Locate platelets.
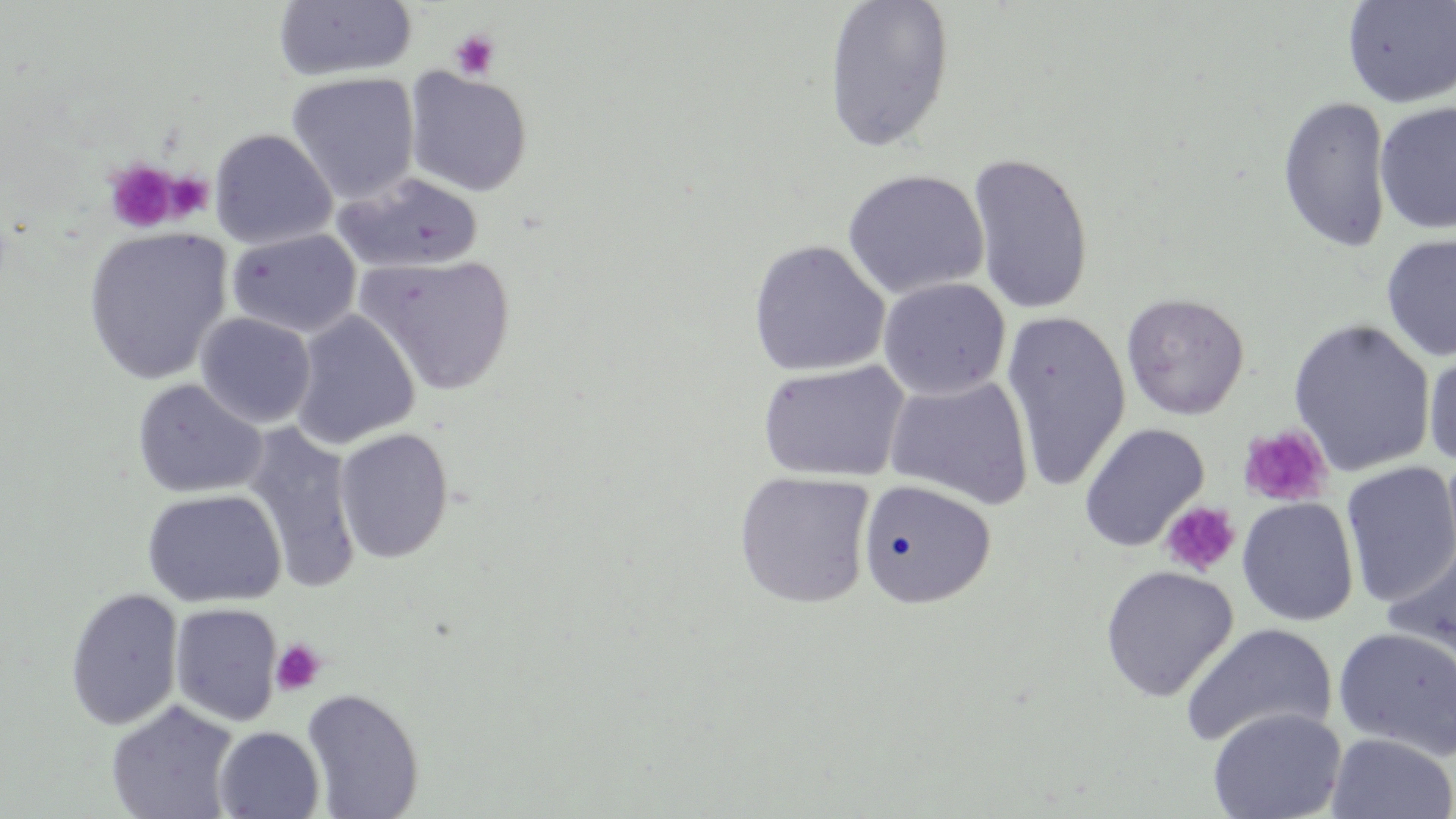
Approximate bounding boxes as named x1/y1/x2/y2 corners in pixels.
Platelets: (x1=448, y1=29, x2=501, y2=81), (x1=104, y1=160, x2=180, y2=233), (x1=165, y1=171, x2=214, y2=220), (x1=1238, y1=423, x2=1332, y2=507), (x1=1161, y1=501, x2=1241, y2=577), (x1=270, y1=638, x2=327, y2=696).

Uninfected red blood cell locations: (x1=822, y1=0, x2=956, y2=153), (x1=1342, y1=0, x2=1456, y2=109), (x1=273, y1=1, x2=418, y2=82), (x1=403, y1=68, x2=533, y2=197), (x1=286, y1=72, x2=421, y2=204), (x1=1277, y1=96, x2=1393, y2=254), (x1=1375, y1=101, x2=1456, y2=235), (x1=210, y1=128, x2=337, y2=250), (x1=966, y1=151, x2=1095, y2=315), (x1=841, y1=168, x2=990, y2=300), (x1=333, y1=171, x2=483, y2=275), (x1=82, y1=226, x2=233, y2=385), (x1=227, y1=228, x2=362, y2=338), (x1=1381, y1=233, x2=1456, y2=363), (x1=748, y1=239, x2=890, y2=377), (x1=354, y1=253, x2=517, y2=395), (x1=877, y1=277, x2=1011, y2=400), (x1=1121, y1=293, x2=1249, y2=420), (x1=290, y1=310, x2=421, y2=450), (x1=195, y1=312, x2=316, y2=428), (x1=1001, y1=312, x2=1132, y2=491), (x1=1288, y1=318, x2=1436, y2=477), (x1=1423, y1=344, x2=1456, y2=472), (x1=757, y1=360, x2=910, y2=484), (x1=884, y1=374, x2=1034, y2=510), (x1=132, y1=378, x2=268, y2=499), (x1=1079, y1=423, x2=1209, y2=552), (x1=241, y1=424, x2=362, y2=591), (x1=333, y1=427, x2=455, y2=563), (x1=1340, y1=461, x2=1456, y2=608), (x1=734, y1=470, x2=876, y2=609), (x1=857, y1=479, x2=997, y2=610), (x1=141, y1=489, x2=286, y2=609), (x1=1236, y1=497, x2=1359, y2=627), (x1=1383, y1=541, x2=1456, y2=669), (x1=1100, y1=565, x2=1238, y2=702), (x1=64, y1=587, x2=184, y2=730), (x1=169, y1=602, x2=283, y2=726), (x1=1180, y1=622, x2=1339, y2=749), (x1=1332, y1=626, x2=1456, y2=761), (x1=300, y1=688, x2=424, y2=818), (x1=105, y1=700, x2=240, y2=819), (x1=1207, y1=707, x2=1347, y2=819), (x1=213, y1=726, x2=325, y2=818), (x1=1326, y1=732, x2=1456, y2=819). Slide-level diagnosis: negative for blood parasites. Thin blood film. 1000x magnification. One field of a larger specimen. Light microscopy. Image is 1456×819 pixels. May-Grünwald-Giemsa-stained preparation.